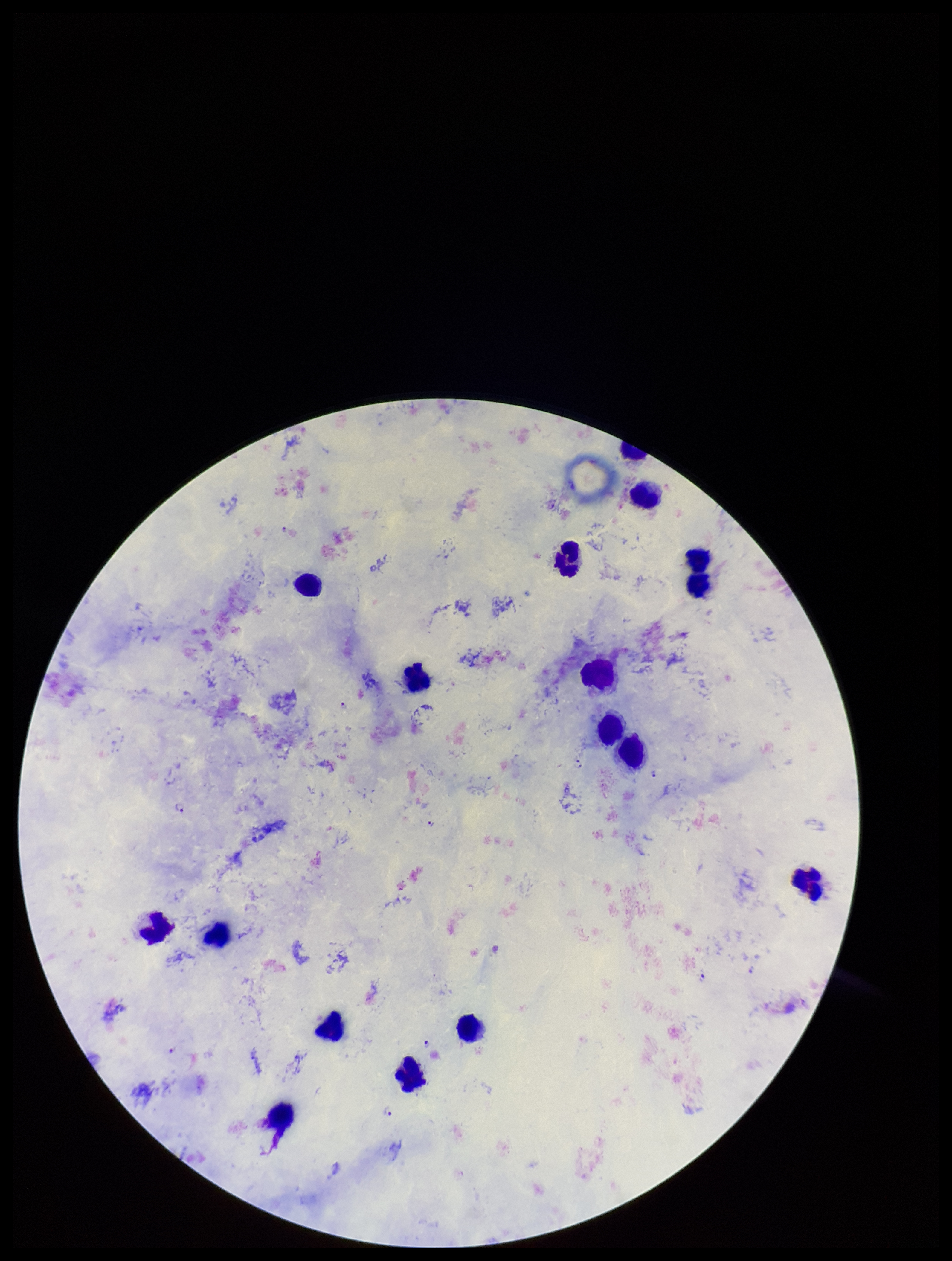
Preparation: thick blood smear. Parasite count: 11. Image is 952×1261 pixels. Photographed through the microscope eyepiece with a smartphone camera. Plasmodium parasites: seen. Patient malaria status: infected. One field from this slide. Leukocyte count: 17. Species reported for this patient: Plasmodium falciparum. Giemsa stain.